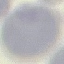

Summary:
  - Malaria status: uninfected
  - Image type: cell patch, automatically extracted from a larger field of view and resized to 64 × 64 pixels
  - Capture: smartphone through the microscope eyepiece
  - Preparation: thin blood smear
  - Stain: Giemsa